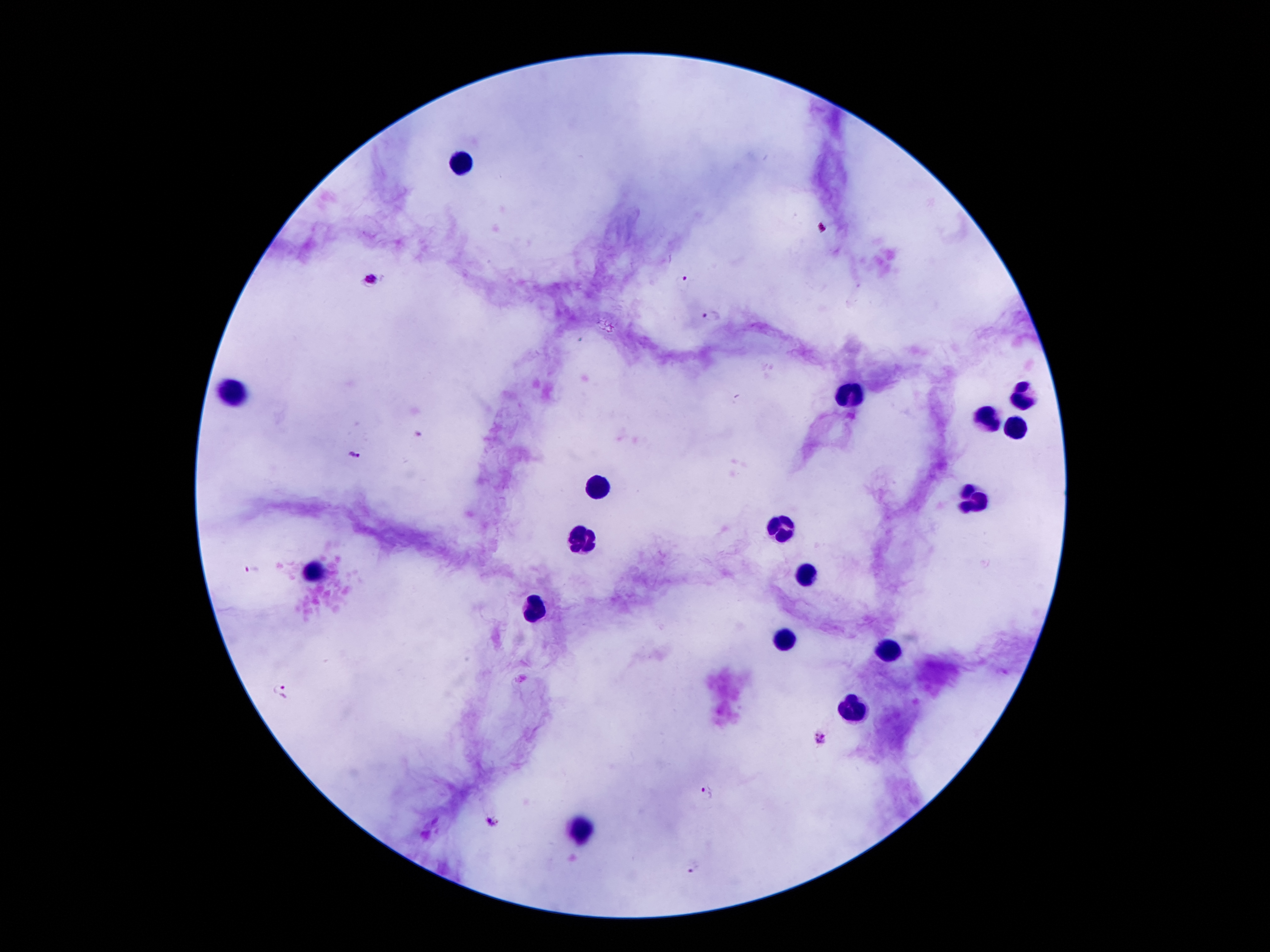 Approximate centers as (x, y) in pixels. Leukocyte locations: (459, 165), (234, 392), (1024, 395), (852, 397), (988, 419), (1015, 429), (599, 488), (972, 497), (784, 524), (579, 538), (313, 572), (804, 577), (536, 610), (783, 640), (890, 651), (851, 711), (581, 829). Malaria parasite locations: (373, 279), (683, 280), (713, 315), (420, 433), (354, 454), (253, 569), (281, 691), (822, 737), (707, 789), (491, 821), (695, 868). Thick peripheral-blood smear. Smartphone photograph taken through the microscope eyepiece. Patient malaria status: infected with Plasmodium falciparum. Image is 1270×952 pixels. Giemsa-stained preparation. 100x magnification. Single field of view.